Identify the cell.
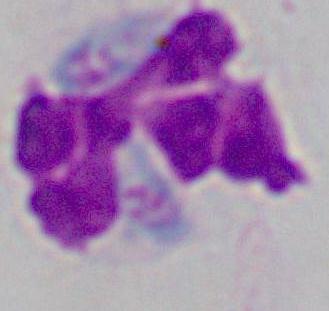
This is a leukocyte.

Summary:
  - Magnification: 1000x
  - Modality: photomicrograph